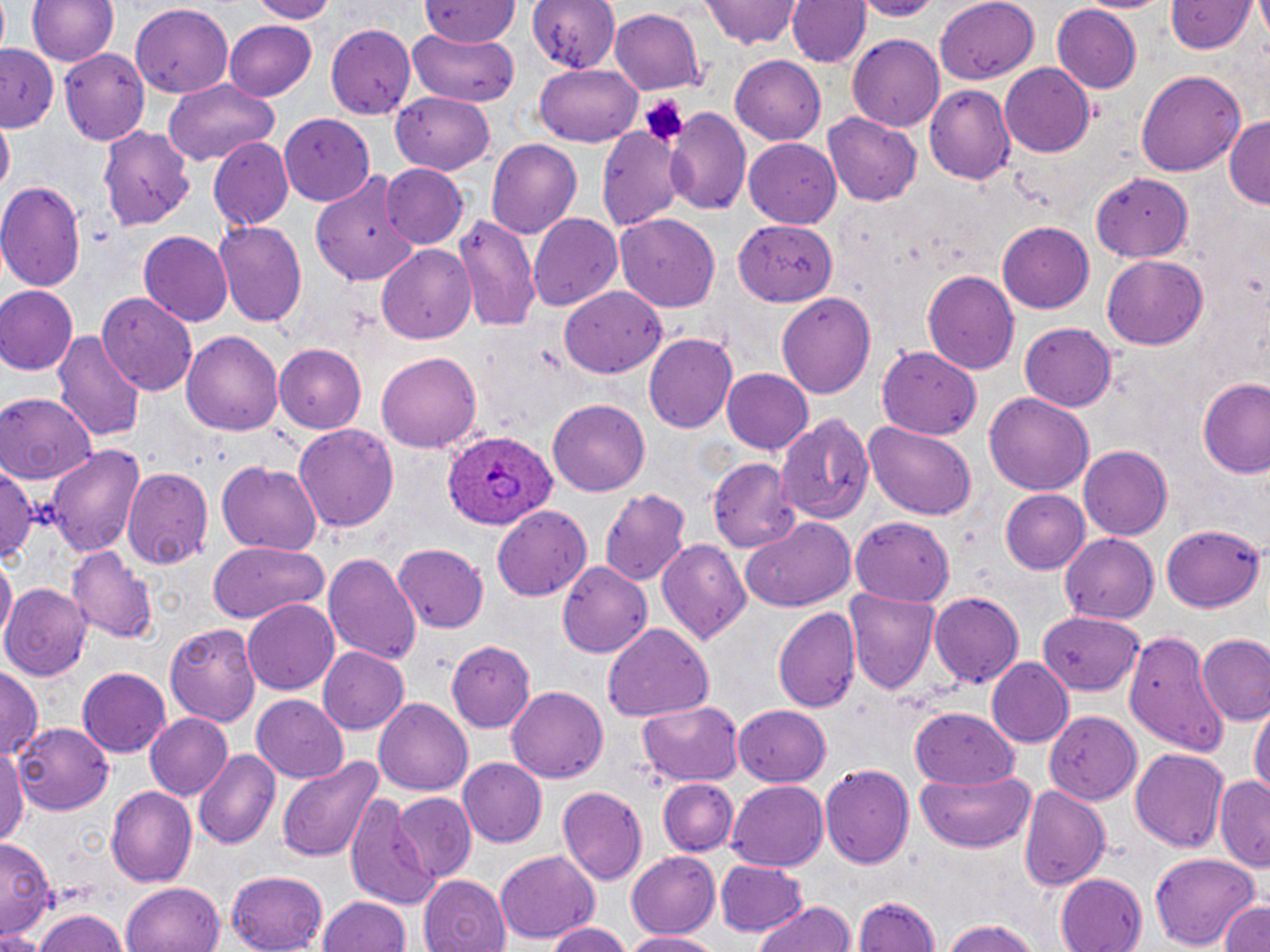
Summary:
  - Coordinate format: approximate bounding boxes as named x1/y1/x2/y2 corners in pixels
  - Uninfected red blood cell locations: (x1=29, y1=0, x2=119, y2=67), (x1=246, y1=0, x2=341, y2=22), (x1=419, y1=0, x2=519, y2=45), (x1=528, y1=0, x2=621, y2=77), (x1=703, y1=0, x2=802, y2=51), (x1=789, y1=0, x2=872, y2=71), (x1=853, y1=0, x2=941, y2=20), (x1=1075, y1=0, x2=1168, y2=14), (x1=938, y1=1, x2=1039, y2=85), (x1=1050, y1=3, x2=1146, y2=91), (x1=1165, y1=3, x2=1257, y2=56), (x1=130, y1=6, x2=234, y2=97), (x1=610, y1=6, x2=707, y2=95), (x1=224, y1=20, x2=318, y2=98), (x1=326, y1=25, x2=418, y2=119), (x1=407, y1=27, x2=519, y2=108), (x1=848, y1=35, x2=944, y2=131), (x1=1, y1=44, x2=60, y2=131), (x1=58, y1=48, x2=151, y2=142), (x1=731, y1=52, x2=828, y2=146), (x1=999, y1=63, x2=1098, y2=156), (x1=535, y1=64, x2=642, y2=146), (x1=1135, y1=70, x2=1246, y2=176), (x1=163, y1=79, x2=281, y2=164), (x1=927, y1=84, x2=1016, y2=184), (x1=392, y1=92, x2=496, y2=175), (x1=665, y1=105, x2=750, y2=215), (x1=823, y1=113, x2=923, y2=206), (x1=281, y1=115, x2=375, y2=205), (x1=1225, y1=115, x2=1270, y2=208), (x1=0, y1=117, x2=15, y2=193), (x1=596, y1=123, x2=684, y2=229), (x1=101, y1=126, x2=195, y2=231), (x1=745, y1=137, x2=844, y2=227), (x1=207, y1=138, x2=293, y2=232), (x1=486, y1=138, x2=582, y2=239), (x1=381, y1=165, x2=468, y2=249), (x1=1091, y1=169, x2=1195, y2=264), (x1=312, y1=173, x2=419, y2=285), (x1=0, y1=179, x2=87, y2=293), (x1=615, y1=212, x2=722, y2=310), (x1=454, y1=214, x2=541, y2=332), (x1=529, y1=214, x2=623, y2=312), (x1=733, y1=218, x2=838, y2=305), (x1=214, y1=220, x2=307, y2=327), (x1=997, y1=221, x2=1094, y2=313), (x1=136, y1=230, x2=233, y2=327), (x1=377, y1=244, x2=477, y2=343), (x1=1102, y1=256, x2=1207, y2=350), (x1=922, y1=270, x2=1019, y2=375), (x1=0, y1=285, x2=78, y2=375), (x1=559, y1=286, x2=667, y2=372), (x1=99, y1=291, x2=199, y2=398), (x1=776, y1=292, x2=879, y2=398), (x1=1020, y1=323, x2=1119, y2=411), (x1=54, y1=327, x2=146, y2=444), (x1=181, y1=331, x2=283, y2=436), (x1=644, y1=333, x2=737, y2=433), (x1=276, y1=344, x2=367, y2=433), (x1=878, y1=345, x2=978, y2=440), (x1=376, y1=350, x2=483, y2=453), (x1=722, y1=368, x2=814, y2=453), (x1=1197, y1=374, x2=1270, y2=479), (x1=0, y1=392, x2=99, y2=482), (x1=984, y1=393, x2=1094, y2=495), (x1=548, y1=398, x2=650, y2=495), (x1=773, y1=413, x2=874, y2=527), (x1=860, y1=420, x2=979, y2=521), (x1=293, y1=422, x2=399, y2=532), (x1=45, y1=442, x2=146, y2=559), (x1=1079, y1=446, x2=1171, y2=538), (x1=706, y1=457, x2=802, y2=553), (x1=1, y1=460, x2=39, y2=568), (x1=216, y1=461, x2=325, y2=556), (x1=123, y1=466, x2=212, y2=571), (x1=599, y1=488, x2=691, y2=584), (x1=999, y1=489, x2=1090, y2=574), (x1=492, y1=503, x2=592, y2=600), (x1=852, y1=517, x2=954, y2=605), (x1=741, y1=518, x2=857, y2=613), (x1=1160, y1=523, x2=1267, y2=612), (x1=1058, y1=532, x2=1159, y2=623), (x1=655, y1=538, x2=752, y2=644), (x1=205, y1=541, x2=330, y2=623), (x1=392, y1=544, x2=488, y2=633), (x1=71, y1=546, x2=156, y2=645), (x1=324, y1=550, x2=422, y2=668), (x1=1, y1=558, x2=14, y2=646), (x1=558, y1=562, x2=653, y2=657), (x1=2, y1=581, x2=93, y2=681), (x1=845, y1=587, x2=942, y2=697), (x1=929, y1=590, x2=1023, y2=691), (x1=243, y1=599, x2=341, y2=697), (x1=774, y1=607, x2=862, y2=717), (x1=1038, y1=612, x2=1146, y2=700), (x1=164, y1=622, x2=262, y2=727), (x1=602, y1=623, x2=715, y2=722), (x1=1119, y1=625, x2=1233, y2=758), (x1=1198, y1=635, x2=1270, y2=726), (x1=446, y1=640, x2=535, y2=732), (x1=316, y1=646, x2=409, y2=736), (x1=986, y1=657, x2=1073, y2=748), (x1=0, y1=664, x2=43, y2=763), (x1=76, y1=667, x2=173, y2=756), (x1=506, y1=686, x2=607, y2=783), (x1=251, y1=694, x2=349, y2=783), (x1=373, y1=697, x2=474, y2=795), (x1=637, y1=702, x2=742, y2=784), (x1=1250, y1=703, x2=1269, y2=802), (x1=733, y1=704, x2=833, y2=786), (x1=907, y1=704, x2=1019, y2=786), (x1=1044, y1=711, x2=1139, y2=804), (x1=144, y1=713, x2=234, y2=801), (x1=14, y1=723, x2=114, y2=813), (x1=0, y1=743, x2=28, y2=848), (x1=1129, y1=746, x2=1229, y2=852), (x1=193, y1=750, x2=280, y2=850), (x1=274, y1=755, x2=386, y2=865), (x1=457, y1=758, x2=547, y2=848), (x1=820, y1=763, x2=913, y2=874), (x1=915, y1=768, x2=1035, y2=853), (x1=1215, y1=777, x2=1269, y2=869), (x1=657, y1=778, x2=736, y2=854), (x1=727, y1=781, x2=829, y2=871), (x1=1019, y1=783, x2=1111, y2=891), (x1=557, y1=785, x2=649, y2=885), (x1=106, y1=786, x2=196, y2=889), (x1=342, y1=793, x2=441, y2=908), (x1=393, y1=794, x2=478, y2=883), (x1=0, y1=837, x2=53, y2=936), (x1=624, y1=850, x2=722, y2=940), (x1=495, y1=852, x2=599, y2=946), (x1=1148, y1=853, x2=1263, y2=948), (x1=714, y1=862, x2=808, y2=935), (x1=227, y1=870, x2=328, y2=952), (x1=1055, y1=872, x2=1148, y2=952), (x1=418, y1=875, x2=513, y2=952), (x1=121, y1=882, x2=226, y2=952), (x1=851, y1=893, x2=944, y2=950), (x1=319, y1=896, x2=412, y2=952), (x1=751, y1=901, x2=856, y2=952), (x1=1219, y1=901, x2=1270, y2=952), (x1=31, y1=910, x2=127, y2=952), (x1=939, y1=918, x2=1045, y2=952), (x1=542, y1=921, x2=629, y2=952), (x1=0, y1=930, x2=47, y2=952), (x1=624, y1=931, x2=727, y2=951)
  - Plasmodium ovale-infected red blood cell locations: (x1=445, y1=426, x2=556, y2=530)
  - Platelet locations: (x1=643, y1=98, x2=685, y2=140)
  - Slide-level diagnosis: Plasmodium ovale
  - Preparation: thin blood film
  - Stain: May-Grünwald-Giemsa
  - Image size: 1270×952 pixels
  - Field of view: single
  - Magnification: 1000x
  - Modality: light microscopy